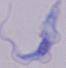

Micrograph. A trypanosome is shown. 1000x magnification.